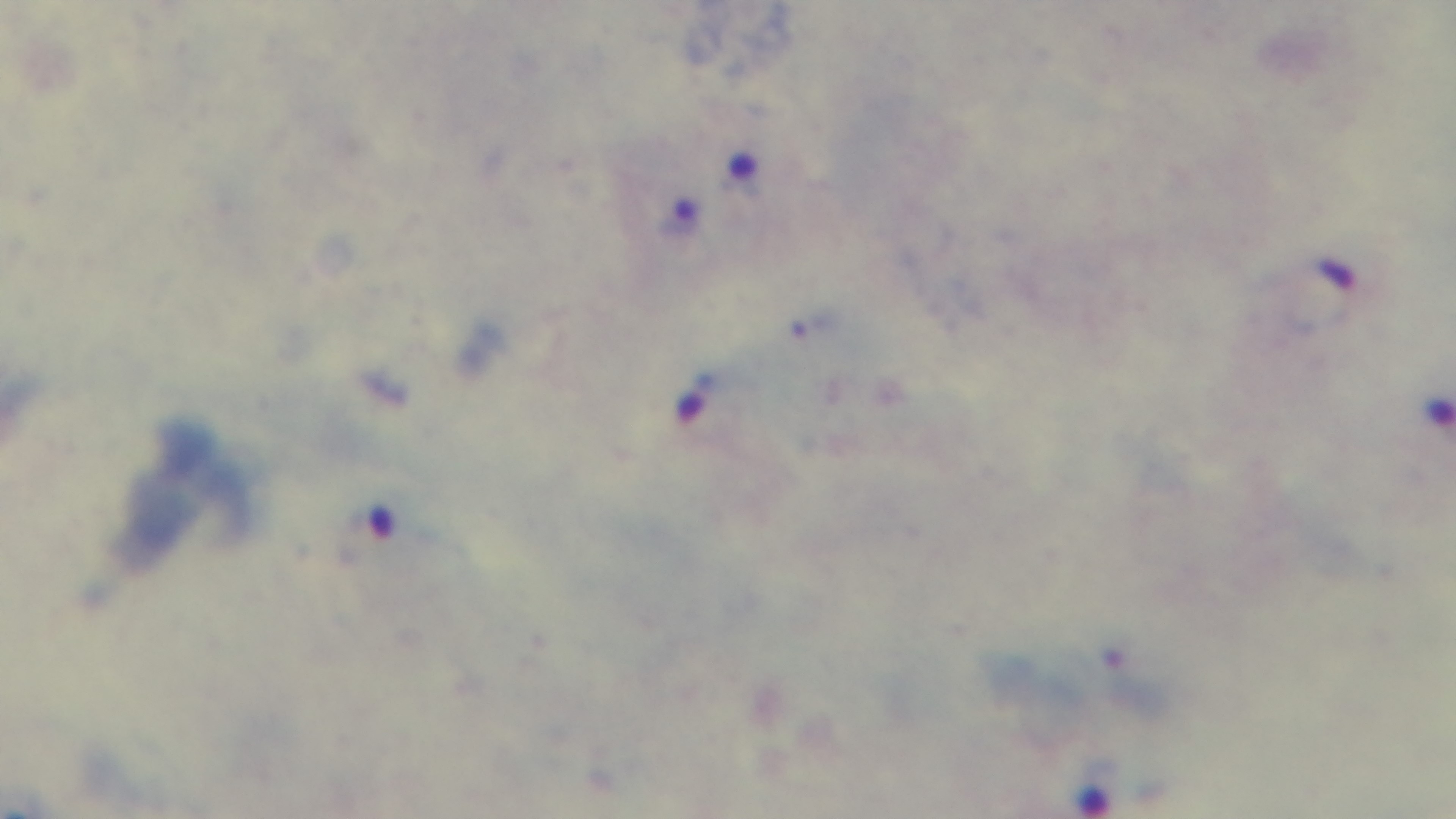

{
  "malaria_status": "positive",
  "preparation": "thick",
  "field_of_view": "single",
  "objective": "100x oil immersion",
  "capture": "mounted 4K digital camera",
  "modality": "light microscopy",
  "stain": "Giemsa"
}